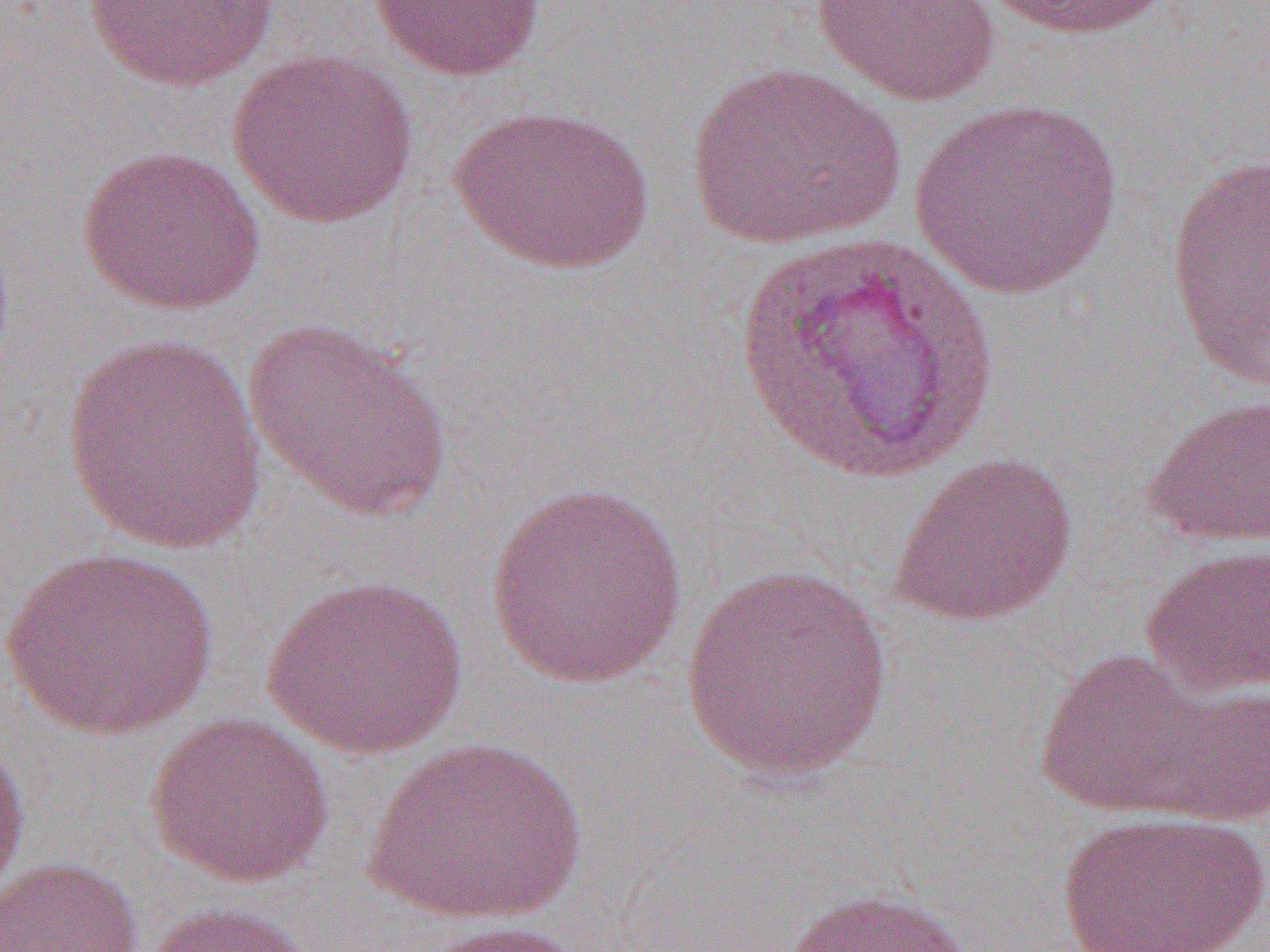

slide-level diagnosis = Plasmodium vivax
image size = 1270×952 pixels
field of view = single
uninfected red blood cell locations = approximate bounding boxes as named x1/y1/x2/y2 corners in pixels: (x1=82, y1=0, x2=280, y2=92), (x1=369, y1=0, x2=546, y2=82), (x1=985, y1=0, x2=1173, y2=41), (x1=810, y1=1, x2=1001, y2=106), (x1=227, y1=48, x2=419, y2=229), (x1=684, y1=60, x2=905, y2=251), (x1=909, y1=97, x2=1125, y2=299), (x1=448, y1=103, x2=656, y2=275), (x1=75, y1=144, x2=266, y2=316), (x1=1166, y1=153, x2=1270, y2=390), (x1=729, y1=232, x2=1002, y2=485), (x1=241, y1=317, x2=453, y2=521), (x1=59, y1=333, x2=269, y2=557), (x1=1141, y1=394, x2=1270, y2=548), (x1=886, y1=452, x2=1078, y2=629), (x1=486, y1=479, x2=687, y2=689), (x1=1139, y1=544, x2=1270, y2=698), (x1=1, y1=546, x2=217, y2=740), (x1=679, y1=562, x2=897, y2=786), (x1=260, y1=574, x2=469, y2=759), (x1=1033, y1=647, x2=1232, y2=820), (x1=1135, y1=676, x2=1270, y2=828), (x1=144, y1=712, x2=336, y2=888), (x1=0, y1=726, x2=31, y2=910), (x1=364, y1=735, x2=586, y2=927), (x1=1053, y1=810, x2=1269, y2=952), (x1=0, y1=856, x2=143, y2=952), (x1=777, y1=885, x2=978, y2=952), (x1=142, y1=901, x2=316, y2=952), (x1=415, y1=920, x2=595, y2=952)
preparation = thin blood smear
magnification = 1000x
modality = light microscopy